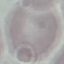
Result: no malaria parasites detected. Thin smear of blood. Photographed with a smartphone camera at the microscope eyepiece. Cell patch, automatically extracted from a larger field of view and resized to 64 × 64 pixels. Giemsa stain.